Name the blood parasite species.
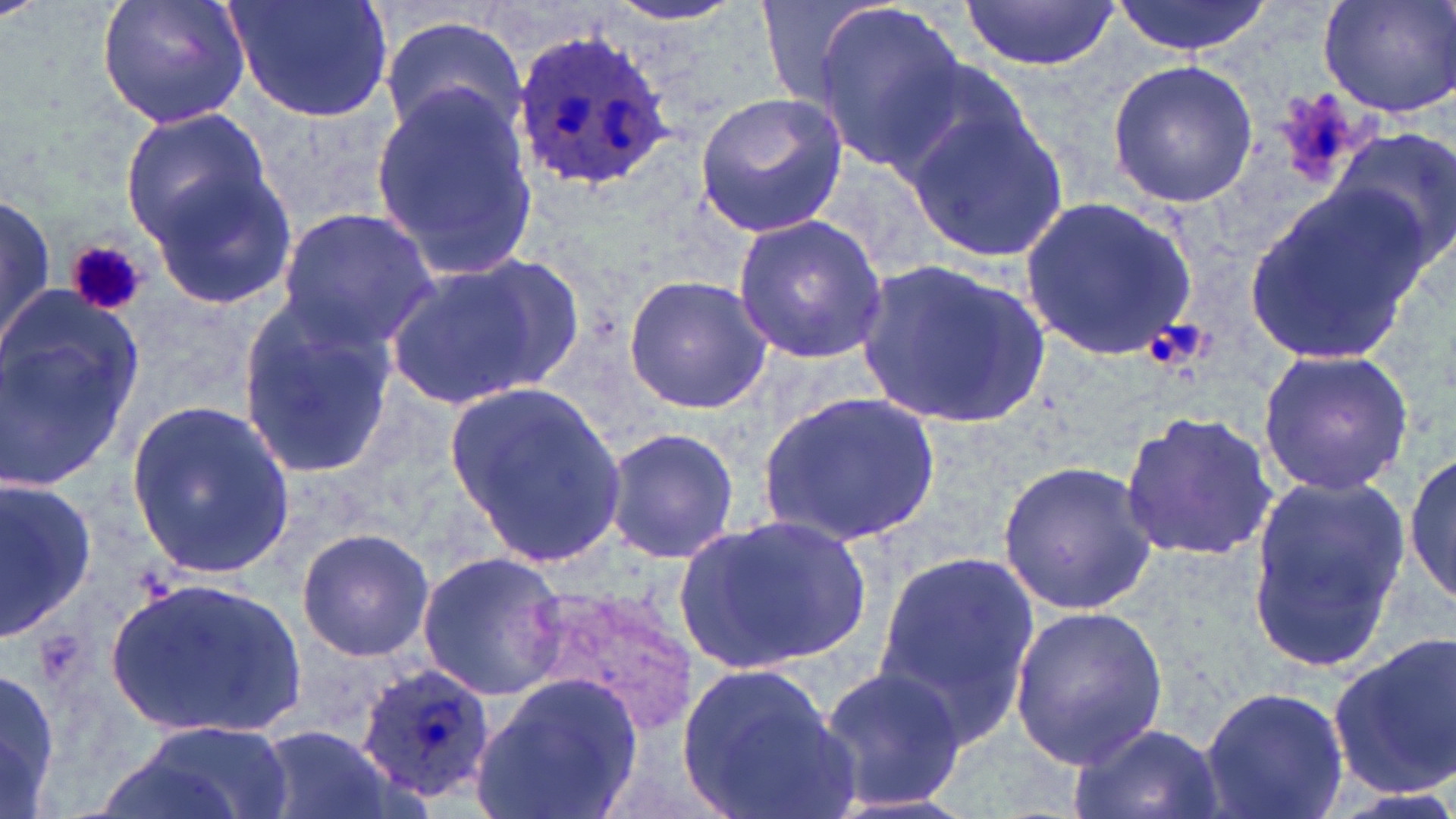

Plasmodium ovale.

Summary:
  - Coordinate format: approximate bounding boxes as named x1/y1/x2/y2 corners in pixels
  - Plasmodium ovale-infected red blood cell locations: (x1=507, y1=24, x2=679, y2=196), (x1=356, y1=660, x2=495, y2=802)
  - Uninfected red blood cell locations: (x1=96, y1=0, x2=251, y2=129), (x1=224, y1=0, x2=397, y2=123), (x1=595, y1=0, x2=755, y2=31), (x1=758, y1=0, x2=887, y2=108), (x1=1110, y1=0, x2=1273, y2=57), (x1=1316, y1=0, x2=1456, y2=120), (x1=960, y1=2, x2=1119, y2=74), (x1=813, y1=3, x2=964, y2=172), (x1=381, y1=15, x2=527, y2=141), (x1=1105, y1=59, x2=1258, y2=209), (x1=884, y1=62, x2=1032, y2=193), (x1=371, y1=86, x2=539, y2=275), (x1=693, y1=91, x2=848, y2=238), (x1=906, y1=103, x2=1068, y2=261), (x1=119, y1=105, x2=275, y2=253), (x1=1327, y1=131, x2=1456, y2=276), (x1=145, y1=165, x2=299, y2=312), (x1=1241, y1=184, x2=1432, y2=369), (x1=0, y1=193, x2=54, y2=353), (x1=1020, y1=198, x2=1199, y2=361), (x1=274, y1=208, x2=440, y2=349), (x1=731, y1=215, x2=889, y2=364), (x1=382, y1=254, x2=579, y2=416), (x1=856, y1=258, x2=1055, y2=431), (x1=621, y1=274, x2=775, y2=413), (x1=235, y1=295, x2=400, y2=481), (x1=0, y1=303, x2=145, y2=492), (x1=1256, y1=348, x2=1415, y2=497), (x1=445, y1=380, x2=629, y2=573), (x1=757, y1=389, x2=942, y2=548), (x1=125, y1=404, x2=298, y2=575), (x1=1119, y1=409, x2=1282, y2=563), (x1=601, y1=423, x2=740, y2=566), (x1=1407, y1=446, x2=1456, y2=609), (x1=996, y1=459, x2=1160, y2=615), (x1=1243, y1=471, x2=1409, y2=669), (x1=0, y1=472, x2=96, y2=639), (x1=678, y1=509, x2=871, y2=675), (x1=296, y1=527, x2=435, y2=661), (x1=414, y1=551, x2=567, y2=699), (x1=872, y1=553, x2=1039, y2=744), (x1=107, y1=576, x2=303, y2=738), (x1=1009, y1=604, x2=1171, y2=770), (x1=1329, y1=631, x2=1456, y2=800), (x1=676, y1=660, x2=855, y2=819), (x1=816, y1=665, x2=965, y2=812), (x1=0, y1=666, x2=61, y2=814), (x1=471, y1=673, x2=645, y2=819), (x1=1198, y1=684, x2=1351, y2=819), (x1=130, y1=719, x2=291, y2=819), (x1=1070, y1=721, x2=1226, y2=819), (x1=253, y1=726, x2=394, y2=819)
  - Platelet locations: (x1=65, y1=239, x2=146, y2=316), (x1=1145, y1=318, x2=1213, y2=371)
  - Field of view: one of a larger specimen
  - Image size: 1456×819 pixels
  - Preparation: thin blood film
  - Stain: May-Grünwald-Giemsa
  - Magnification: 1000x
  - Modality: light microscopy